State which parasite is depicted.
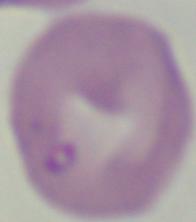
Babesia.

Captured at 1000x magnification. Photomicrograph.